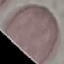

result = no malaria parasites seen
capture = smartphone camera at the microscope eyepiece
preparation = thin smear
image type = automatically extracted cell patch, resized to 64 × 64 pixels
stain = Giemsa